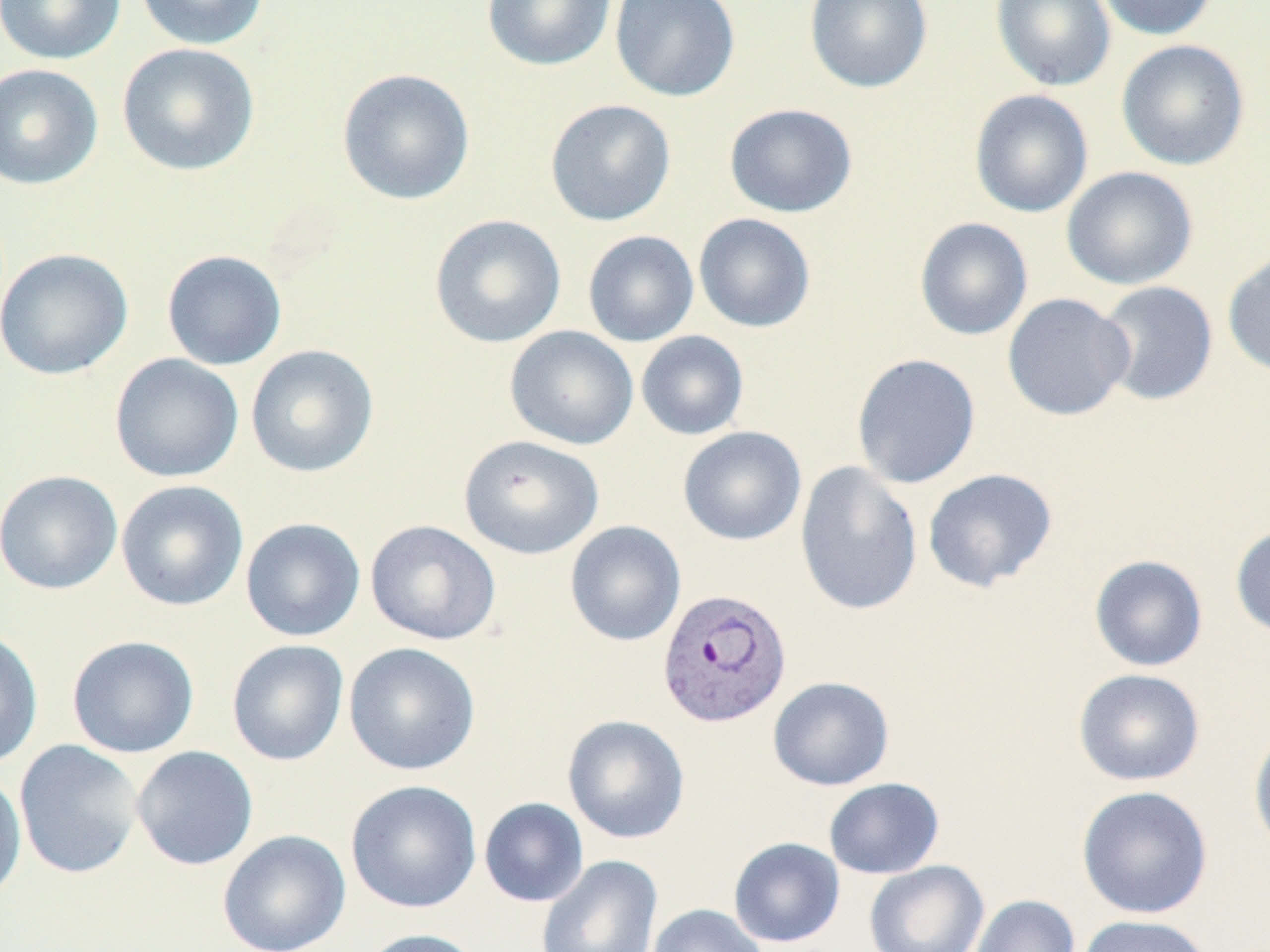
Summary:
  - Coordinate format: approximate bounding boxes as [x1, y1, x2, y2] in pixels
  - Uninfected red blood cell locations: [0, 0, 126, 65], [133, 0, 270, 50], [481, 0, 616, 72], [609, 0, 740, 102], [804, 0, 933, 93], [990, 0, 1116, 91], [1094, 0, 1219, 41], [1116, 39, 1250, 171], [116, 42, 260, 176], [0, 63, 103, 190], [337, 68, 476, 205], [969, 89, 1094, 218], [544, 98, 676, 226], [724, 103, 858, 218], [1061, 166, 1199, 290], [429, 213, 566, 348], [694, 213, 816, 333], [914, 217, 1033, 341], [582, 230, 699, 347], [0, 248, 134, 380], [162, 249, 287, 370], [1222, 249, 1270, 378], [1094, 280, 1219, 406], [1002, 293, 1135, 421], [504, 325, 639, 450], [636, 330, 749, 441], [245, 344, 379, 477], [109, 353, 244, 483], [851, 353, 981, 489], [677, 426, 807, 546], [458, 435, 604, 560], [794, 460, 924, 616], [922, 468, 1058, 593], [0, 469, 123, 595], [115, 480, 249, 611], [240, 517, 366, 642], [365, 519, 501, 645], [565, 520, 686, 647], [1230, 523, 1270, 640], [1089, 555, 1208, 672], [0, 628, 44, 769], [66, 635, 199, 758], [227, 639, 349, 766], [344, 641, 481, 775], [1073, 668, 1206, 786], [767, 676, 894, 790], [562, 714, 690, 844], [1249, 724, 1270, 857], [14, 739, 144, 879], [131, 745, 258, 871], [0, 768, 27, 905], [824, 777, 944, 879], [345, 779, 482, 913], [1076, 785, 1213, 919], [479, 797, 588, 907], [217, 829, 351, 952], [728, 837, 845, 947], [535, 855, 663, 951], [864, 860, 990, 952], [969, 894, 1080, 952], [647, 903, 767, 952], [1075, 915, 1214, 952], [355, 928, 487, 952]
  - Plasmodium vivax-infected red blood cell locations: [656, 587, 792, 728]
  - Slide-level diagnosis: Plasmodium vivax
  - Image size: 1270×952 pixels
  - Field of view: single
  - Preparation: thin blood smear
  - Stain: May-Grünwald-Giemsa
  - Modality: optical microscopy
  - Magnification: 1000x